Classify the preparation.
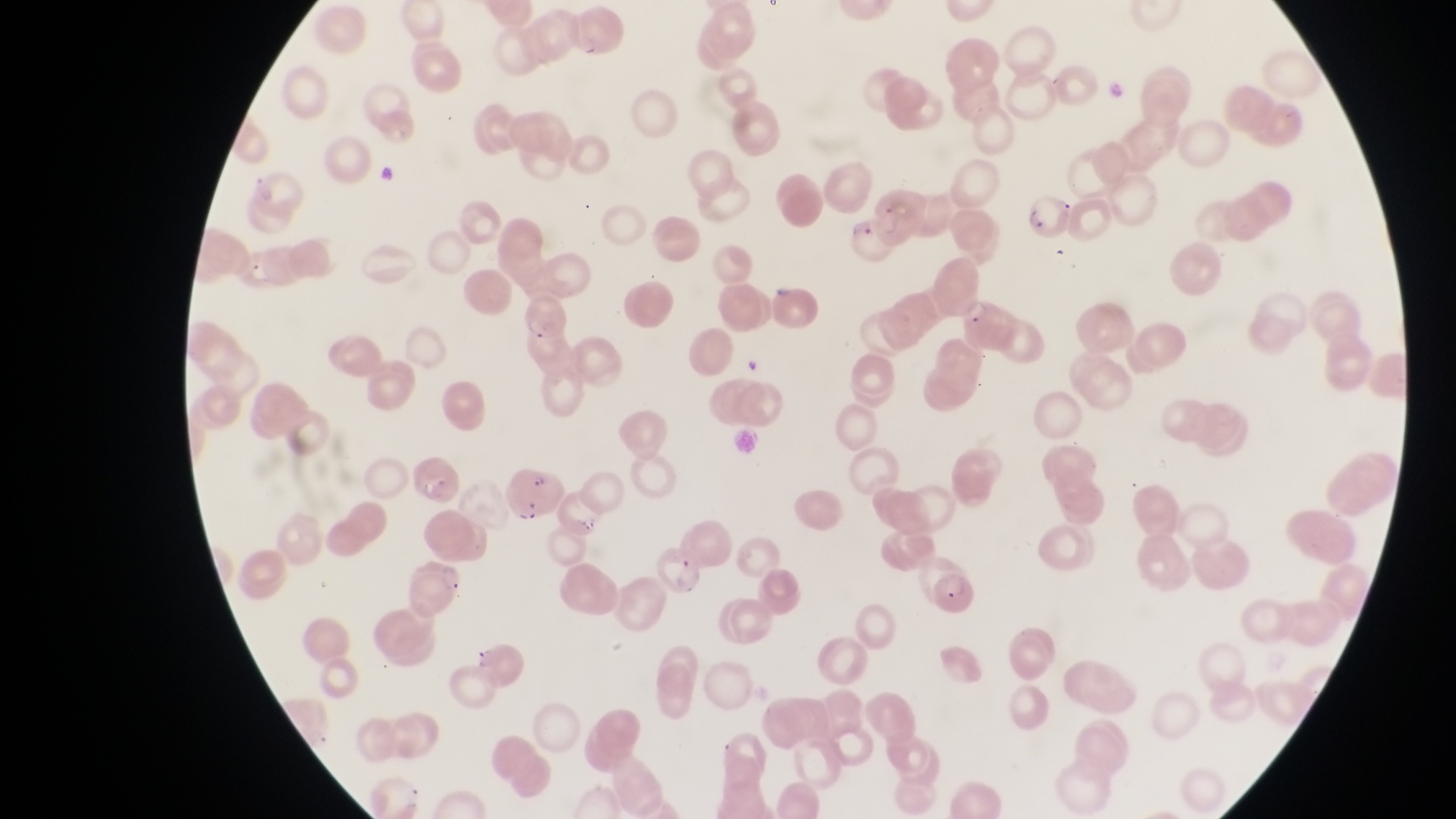
Thin blood film.

Approximate bounding boxes as [left, top, right, bottom] in pixels. Artifact (platelet-like body, stain precipitate, or debris) locations: [376, 165, 403, 191]. Parasitised red blood cell locations: [1026, 190, 1073, 246], [845, 215, 900, 268], [518, 293, 571, 349], [959, 296, 1011, 351], [502, 466, 568, 524], [927, 571, 976, 617], [466, 637, 525, 686]. Image is 1456×819 pixels. Photographed through the eyepiece of an Olympus CX-23 microscope with a smartphone camera. Magnification of 1000x. Collected in Uganda. One field of view.